Identify the blood parasite species.
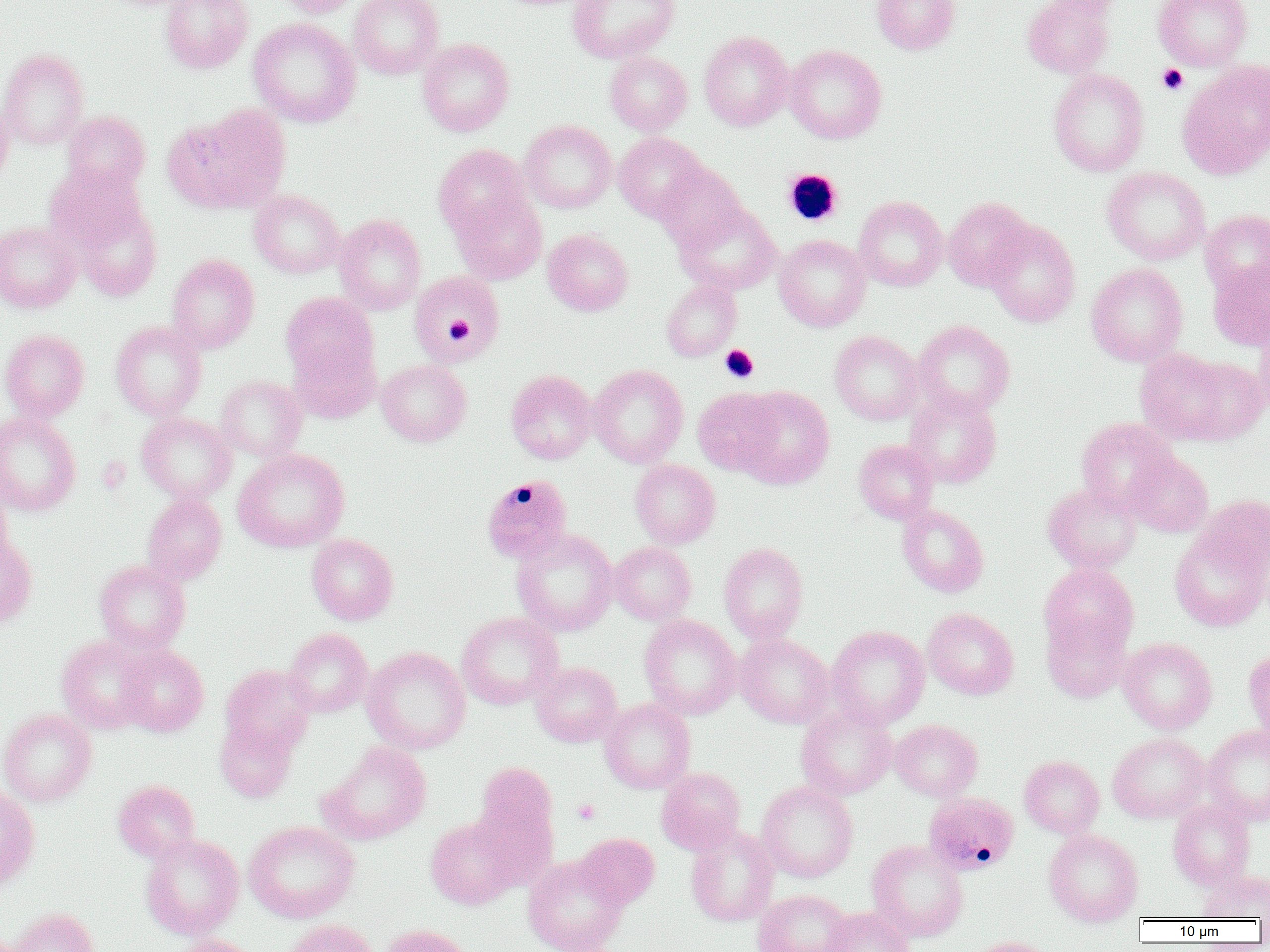

Plasmodium malariae.

{
  "uninfected_red_blood_cell_locations": "approximate bounding boxes as named x1/y1/x2/y2 corners in pixels: (x1=160, y1=0, x2=253, y2=74), (x1=276, y1=0, x2=365, y2=18), (x1=349, y1=0, x2=443, y2=79), (x1=567, y1=0, x2=679, y2=63), (x1=872, y1=0, x2=960, y2=54), (x1=1022, y1=0, x2=1117, y2=79), (x1=1153, y1=0, x2=1253, y2=70), (x1=249, y1=18, x2=360, y2=127), (x1=699, y1=30, x2=794, y2=131), (x1=417, y1=38, x2=515, y2=136), (x1=784, y1=45, x2=887, y2=144), (x1=0, y1=49, x2=89, y2=150), (x1=605, y1=52, x2=692, y2=135), (x1=1177, y1=60, x2=1270, y2=179), (x1=1048, y1=68, x2=1150, y2=177), (x1=0, y1=99, x2=14, y2=190), (x1=166, y1=105, x2=291, y2=213), (x1=62, y1=110, x2=151, y2=194), (x1=519, y1=120, x2=617, y2=214), (x1=614, y1=132, x2=707, y2=222), (x1=433, y1=144, x2=532, y2=239), (x1=656, y1=162, x2=746, y2=251), (x1=45, y1=163, x2=147, y2=253), (x1=1102, y1=167, x2=1210, y2=265), (x1=248, y1=189, x2=345, y2=278), (x1=451, y1=193, x2=547, y2=284), (x1=854, y1=196, x2=948, y2=290), (x1=943, y1=197, x2=1034, y2=290), (x1=70, y1=200, x2=162, y2=301), (x1=675, y1=203, x2=781, y2=295), (x1=1200, y1=209, x2=1270, y2=298), (x1=334, y1=214, x2=426, y2=314), (x1=984, y1=220, x2=1081, y2=328), (x1=0, y1=221, x2=81, y2=312), (x1=542, y1=229, x2=633, y2=316), (x1=774, y1=234, x2=870, y2=331), (x1=167, y1=253, x2=260, y2=353), (x1=1208, y1=259, x2=1270, y2=351), (x1=1086, y1=263, x2=1188, y2=366), (x1=409, y1=271, x2=505, y2=365), (x1=661, y1=280, x2=741, y2=361), (x1=280, y1=292, x2=378, y2=386), (x1=1253, y1=319, x2=1270, y2=418), (x1=111, y1=320, x2=206, y2=420), (x1=913, y1=320, x2=1015, y2=418), (x1=0, y1=328, x2=90, y2=421), (x1=829, y1=330, x2=923, y2=425), (x1=288, y1=338, x2=380, y2=423), (x1=1136, y1=348, x2=1258, y2=446), (x1=376, y1=359, x2=471, y2=446), (x1=588, y1=365, x2=688, y2=467), (x1=506, y1=370, x2=597, y2=464), (x1=216, y1=375, x2=307, y2=461), (x1=735, y1=387, x2=834, y2=490), (x1=692, y1=388, x2=780, y2=476), (x1=903, y1=389, x2=1002, y2=488), (x1=0, y1=411, x2=81, y2=516), (x1=136, y1=412, x2=235, y2=504), (x1=1075, y1=418, x2=1178, y2=513), (x1=854, y1=439, x2=938, y2=523), (x1=233, y1=449, x2=350, y2=552), (x1=1126, y1=453, x2=1213, y2=537), (x1=630, y1=459, x2=721, y2=548), (x1=1043, y1=483, x2=1142, y2=574), (x1=0, y1=485, x2=14, y2=570), (x1=142, y1=493, x2=227, y2=585), (x1=1196, y1=494, x2=1270, y2=578), (x1=898, y1=504, x2=988, y2=597), (x1=512, y1=528, x2=618, y2=637), (x1=1169, y1=528, x2=1269, y2=631), (x1=306, y1=533, x2=398, y2=625), (x1=0, y1=534, x2=37, y2=630), (x1=609, y1=542, x2=696, y2=625), (x1=719, y1=542, x2=808, y2=643), (x1=94, y1=559, x2=190, y2=653), (x1=1039, y1=562, x2=1139, y2=658), (x1=922, y1=608, x2=1019, y2=700), (x1=456, y1=612, x2=564, y2=710), (x1=639, y1=615, x2=741, y2=719), (x1=1042, y1=616, x2=1131, y2=702), (x1=827, y1=625, x2=930, y2=729), (x1=284, y1=627, x2=373, y2=717), (x1=735, y1=633, x2=834, y2=728), (x1=56, y1=635, x2=154, y2=733), (x1=1118, y1=637, x2=1217, y2=734), (x1=117, y1=644, x2=208, y2=736), (x1=362, y1=646, x2=471, y2=754), (x1=1244, y1=648, x2=1270, y2=738), (x1=531, y1=662, x2=622, y2=747), (x1=220, y1=664, x2=315, y2=755), (x1=599, y1=699, x2=695, y2=794), (x1=796, y1=704, x2=897, y2=800), (x1=0, y1=708, x2=97, y2=807), (x1=215, y1=717, x2=298, y2=802), (x1=890, y1=720, x2=982, y2=801), (x1=1203, y1=725, x2=1270, y2=824), (x1=1107, y1=732, x2=1209, y2=823), (x1=320, y1=742, x2=431, y2=844), (x1=1019, y1=756, x2=1104, y2=839), (x1=472, y1=764, x2=560, y2=884), (x1=656, y1=767, x2=745, y2=854), (x1=113, y1=779, x2=200, y2=862), (x1=756, y1=781, x2=858, y2=882), (x1=0, y1=786, x2=40, y2=890), (x1=1168, y1=800, x2=1255, y2=890), (x1=425, y1=816, x2=518, y2=910), (x1=244, y1=821, x2=360, y2=923), (x1=685, y1=824, x2=779, y2=927), (x1=1043, y1=829, x2=1143, y2=926), (x1=140, y1=833, x2=244, y2=941), (x1=575, y1=833, x2=659, y2=908), (x1=866, y1=839, x2=968, y2=942), (x1=523, y1=855, x2=628, y2=952), (x1=1199, y1=871, x2=1270, y2=921), (x1=752, y1=889, x2=853, y2=952), (x1=8, y1=907, x2=99, y2=952), (x1=821, y1=907, x2=916, y2=952), (x1=284, y1=919, x2=379, y2=952), (x1=380, y1=924, x2=475, y2=952), (x1=166, y1=935, x2=263, y2=952), (x1=964, y1=937, x2=1056, y2=952)",
  "preparation": "thin blood film",
  "plasmodium_malariae_infected_red_blood_cell_locations": "approximate bounding boxes as named x1/y1/x2/y2 corners in pixels: (x1=481, y1=475, x2=573, y2=564), (x1=924, y1=791, x2=1019, y2=875)",
  "modality": "optical microscopy",
  "field_of_view": "one of a larger specimen",
  "platelet_locations": "approximate bounding boxes as named x1/y1/x2/y2 corners in pixels: (x1=1156, y1=64, x2=1189, y2=95), (x1=783, y1=168, x2=843, y2=226), (x1=444, y1=316, x2=474, y2=341), (x1=719, y1=345, x2=759, y2=383), (x1=573, y1=799, x2=600, y2=825)",
  "image_size": "1270×952 pixels",
  "magnification": "1000x"
}